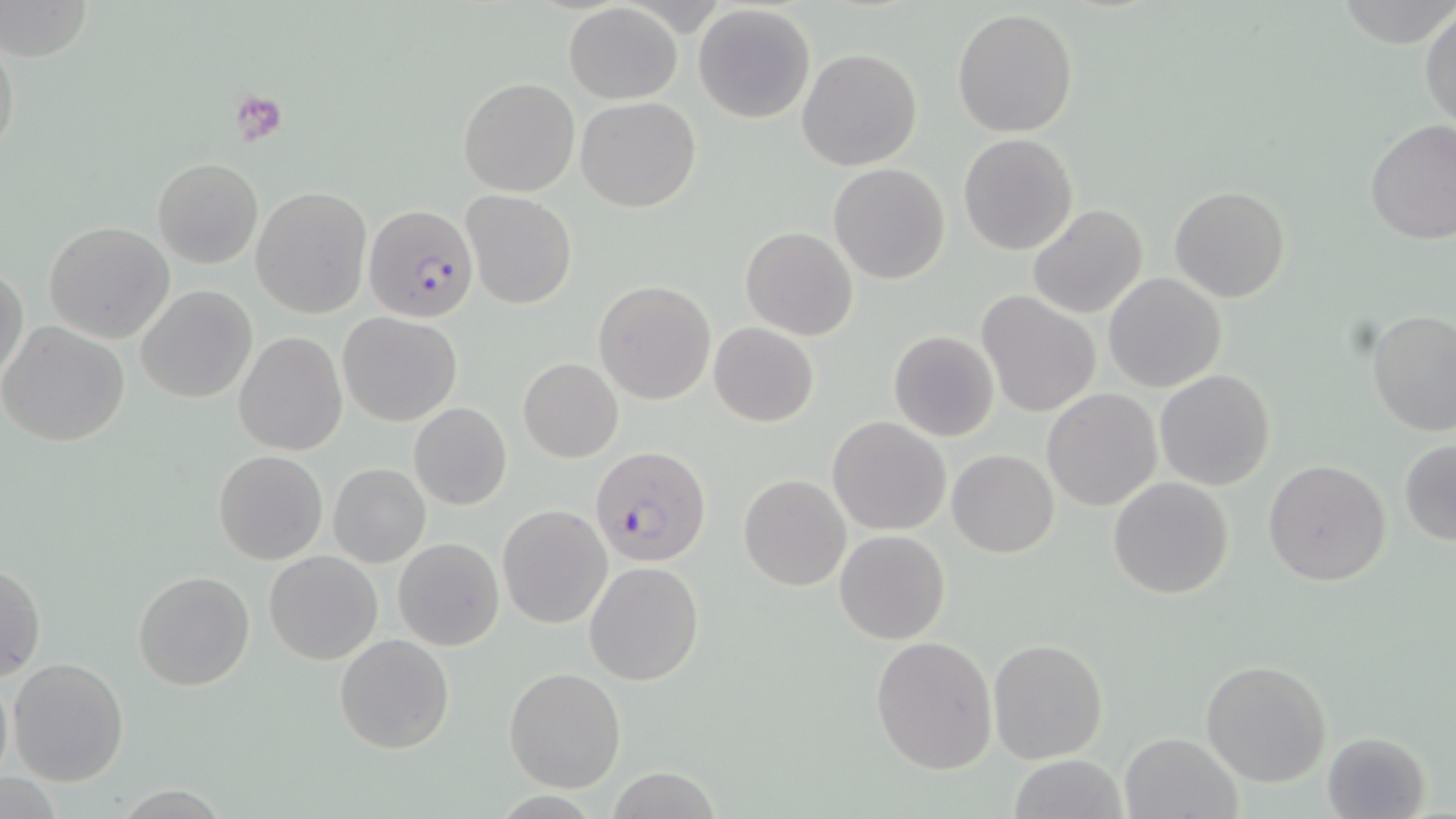

{
  "slide_level_diagnosis": "Plasmodium falciparum",
  "field_of_view": "one of a larger specimen",
  "plasmodium_falciparum_infected_red_blood_cell_locations": "approximate bounding boxes as [x1, y1, x2, y2] in pixels: [363, 203, 482, 326], [590, 443, 711, 567]",
  "stain": "May-Grünwald-Giemsa",
  "magnification": "1000x",
  "preparation": "thin blood smear",
  "modality": "light microscopy",
  "uninfected_red_blood_cell_locations": "approximate bounding boxes as [x1, y1, x2, y2] in pixels: [0, 0, 93, 64], [1336, 0, 1456, 48], [564, 2, 682, 105], [693, 4, 817, 125], [952, 8, 1078, 139], [1420, 8, 1455, 132], [1, 27, 21, 170], [797, 48, 923, 172], [458, 76, 580, 196], [575, 96, 701, 212], [1365, 119, 1456, 244], [958, 132, 1079, 256], [152, 157, 264, 268], [829, 165, 950, 284], [1170, 185, 1290, 302], [252, 186, 373, 319], [460, 190, 577, 310], [1027, 204, 1148, 317], [44, 220, 175, 343], [1011, 221, 1129, 386], [740, 226, 858, 341], [1, 262, 28, 386], [1102, 272, 1227, 393], [594, 279, 716, 404], [135, 284, 257, 403], [978, 291, 1098, 417], [1366, 309, 1456, 439], [340, 313, 461, 426], [0, 321, 131, 447], [709, 322, 819, 426], [233, 331, 348, 455], [887, 331, 999, 442], [518, 358, 623, 462], [1154, 369, 1276, 492], [1042, 389, 1163, 512], [409, 402, 512, 510], [828, 416, 950, 535], [1398, 440, 1456, 544], [948, 449, 1059, 558], [213, 450, 328, 564], [1264, 459, 1391, 586], [327, 464, 430, 567], [740, 474, 851, 591], [1107, 477, 1234, 601], [498, 505, 610, 628], [834, 530, 951, 645], [394, 538, 504, 650], [264, 550, 383, 664], [1, 560, 46, 683], [584, 561, 705, 685], [133, 571, 255, 692], [335, 633, 454, 753], [870, 635, 998, 772], [988, 638, 1109, 764], [7, 657, 130, 786], [1201, 660, 1332, 786], [503, 667, 628, 793], [0, 669, 14, 788], [1121, 732, 1241, 818], [1321, 732, 1433, 819], [1006, 756, 1133, 818]",
  "image_size": "1456×819 pixels",
  "platelet_locations": "approximate bounding boxes as [x1, y1, x2, y2] in pixels: [230, 92, 286, 143]"
}